Outline each blood parasite and name the species.
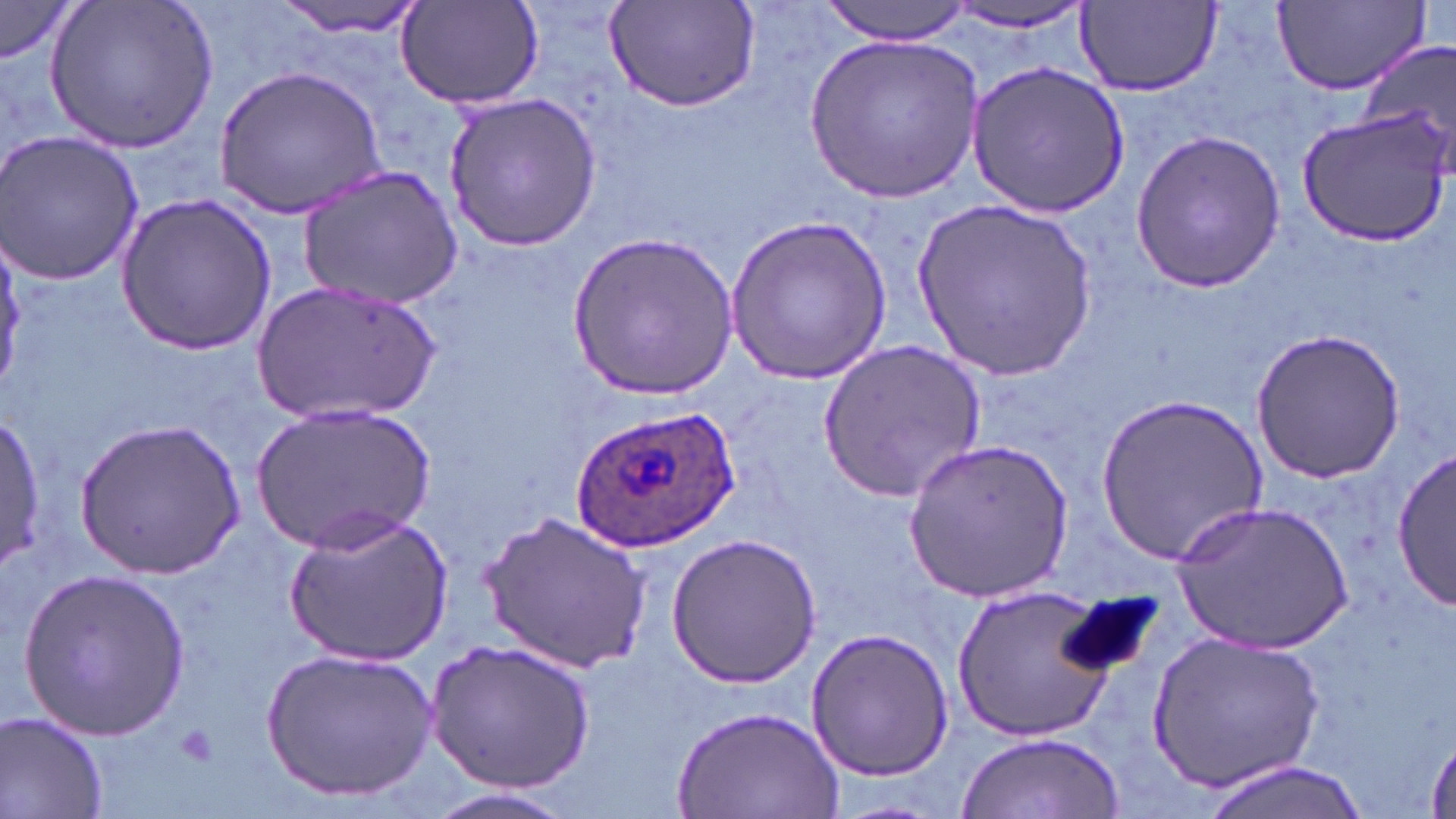
Approximate bounding boxes as (x1,y1)-(x2,y2) corner pairs in pixels.
Plasmodium ovale-infected red blood cells: (568,404)-(742,554).
No Plasmodium falciparum, Plasmodium malariae, Plasmodium vivax, Babesia divergens, or Trypanosoma brucei observed.

Platelet locations: (176,724)-(217,769). Uninfected red blood cell locations: (45,0)-(220,153), (276,0)-(426,40), (393,0)-(544,112), (602,0)-(762,114), (820,0)-(976,44), (1270,0)-(1433,98), (0,2)-(78,67), (1076,2)-(1223,95), (942,5)-(1094,33), (1355,33)-(1456,179), (807,34)-(983,204), (965,62)-(1129,219), (216,67)-(389,218), (443,91)-(603,252), (1297,108)-(1452,245), (1130,128)-(1286,294), (0,129)-(145,288), (298,165)-(462,310), (115,191)-(276,354), (916,198)-(1098,381), (726,211)-(892,382), (567,230)-(738,401), (254,279)-(443,425), (1248,327)-(1406,484), (816,339)-(987,504), (1098,391)-(1269,563), (253,402)-(437,552), (0,414)-(46,572), (75,418)-(244,576), (904,437)-(1075,603), (1392,441)-(1453,612), (1173,501)-(1354,654), (283,507)-(453,668), (477,511)-(651,674), (666,533)-(821,688), (17,565)-(191,741), (952,585)-(1118,741), (806,626)-(956,781), (1146,630)-(1323,791), (427,637)-(595,793), (261,646)-(438,802), (673,701)-(845,819), (0,709)-(111,819), (957,731)-(1124,818), (1426,734)-(1455,819), (1197,760)-(1367,819), (418,786)-(581,819). Slide-level diagnosis: Plasmodium ovale. One field of a larger specimen. Thin blood smear. May-Grünwald-Giemsa stain. Image is 1456×819 pixels. Captured at 1000x magnification. Optical microscopy.